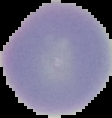
Cell region segmented out of the field of view; the surrounding area is masked to black. Result: no Plasmodium parasites seen. Image is 112×118 pixels. From a thin blood film.